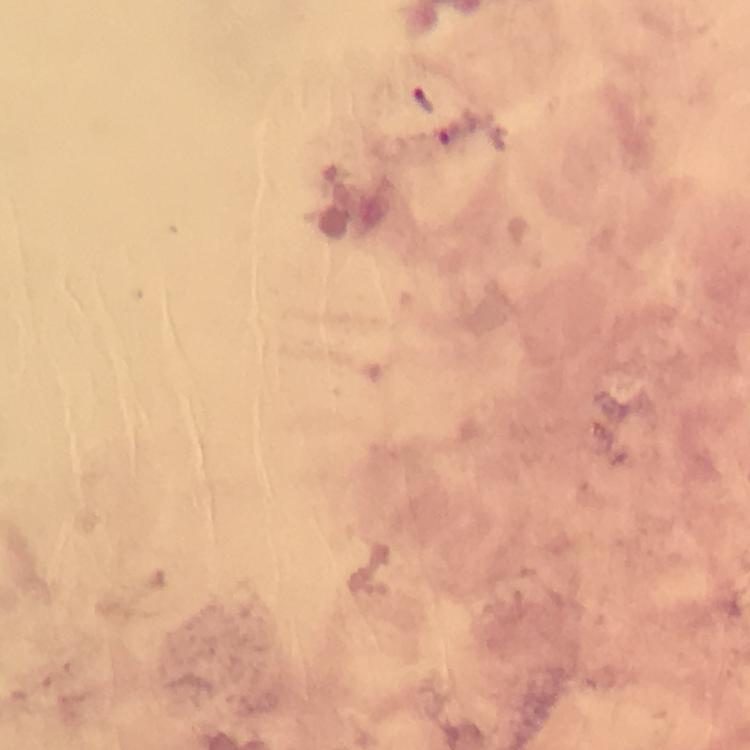

Approximate centers as (x, y) in pixels.
Summary:
  - Plasmodium parasite locations: (424, 102)
  - Stain: Giemsa
  - Preparation: thick smear
  - Context: from a malaria diagnostic workup
  - Capture: smartphone mounted on the microscope
  - Magnification: 100x
  - Image size: 750×750 pixels
  - Immersion oil: applied
  - Cropped from: one field of view